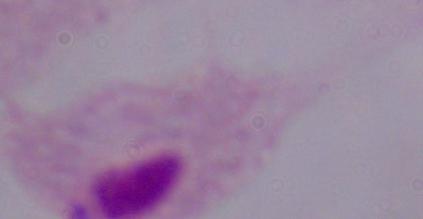

identification = trichomonad
modality = photomicrograph
magnification = 1000x